Give the position of every malaria parasite.
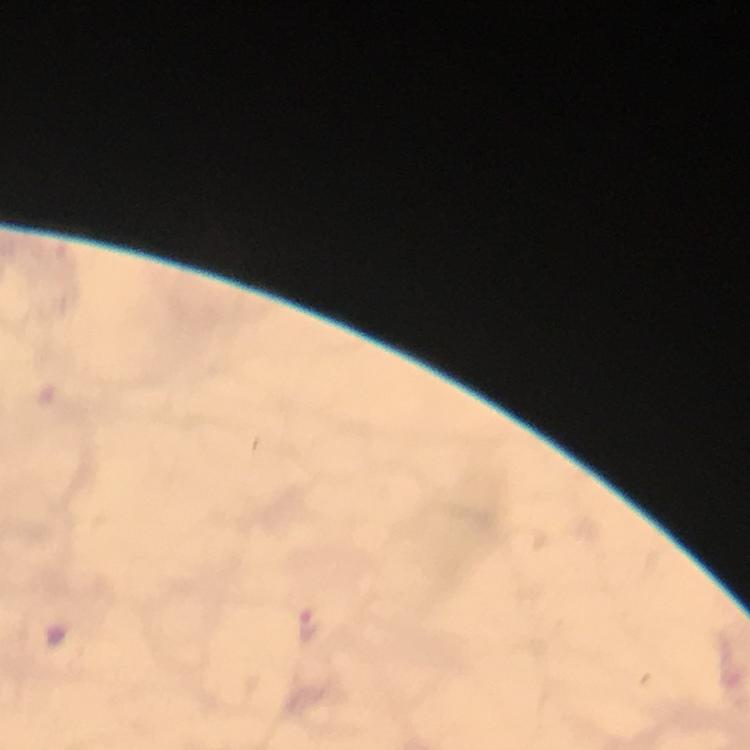
Approximate centers as [x, y] in pixels.
Malaria parasites: [307, 624].

cropped from = a single field of view
immersion oil = applied
preparation = thick smear
context = from a diagnostic examination for malaria
stain = Giemsa
capture = smartphone photograph through a microscope
image size = 750×750 pixels
magnification = 100x